State the preparation type.
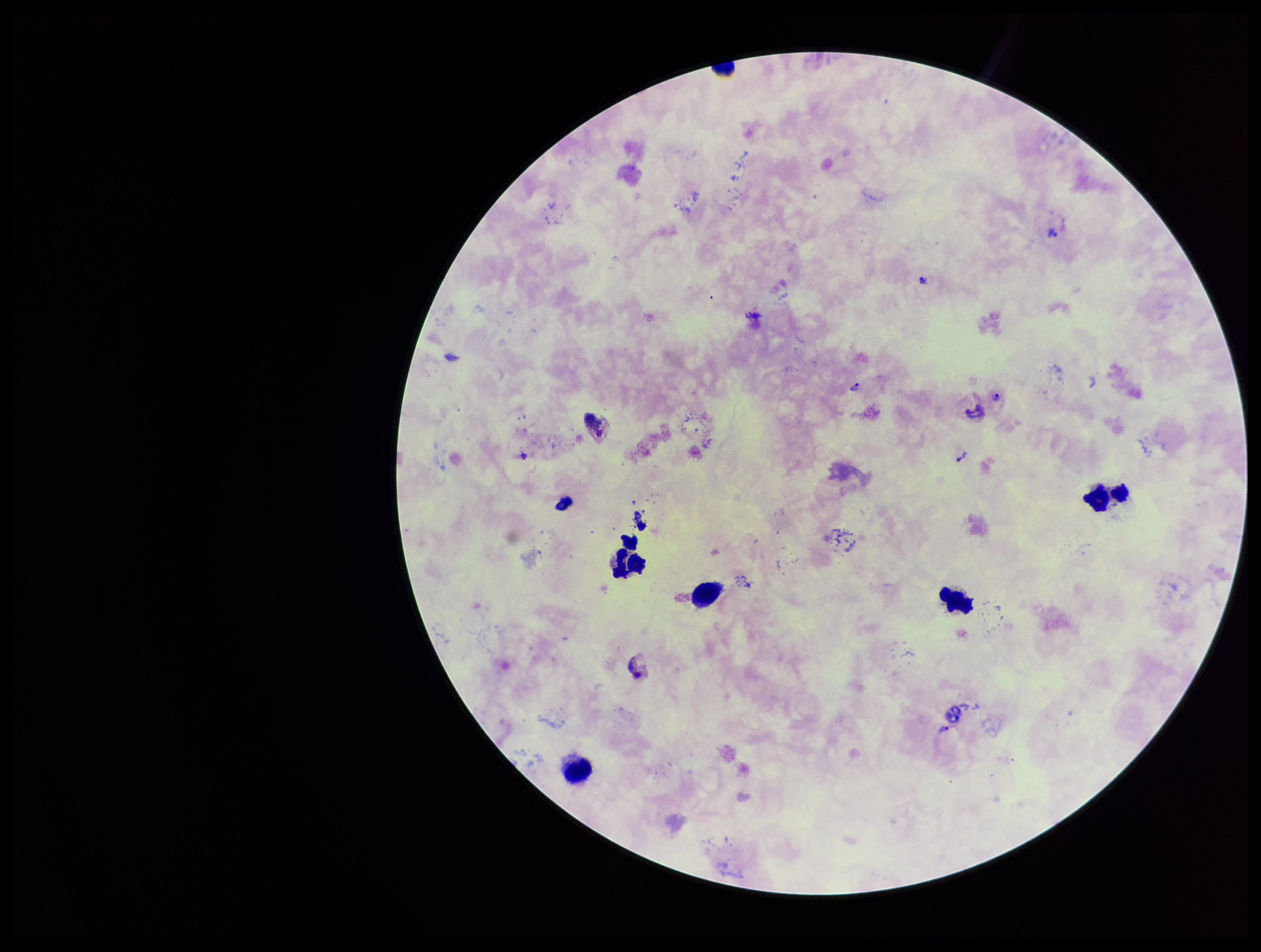

Thick.

Smartphone photograph taken through the eyepiece of a microscope. Image is 1261×952 pixels. Leukocyte count: 6. Species reported for this patient: Plasmodium vivax. Patient malaria status: positive. Parasite count: 6. One field from this slide. Plasmodium parasites: identified. Stained with Giemsa.